Locate and identify every blood parasite.
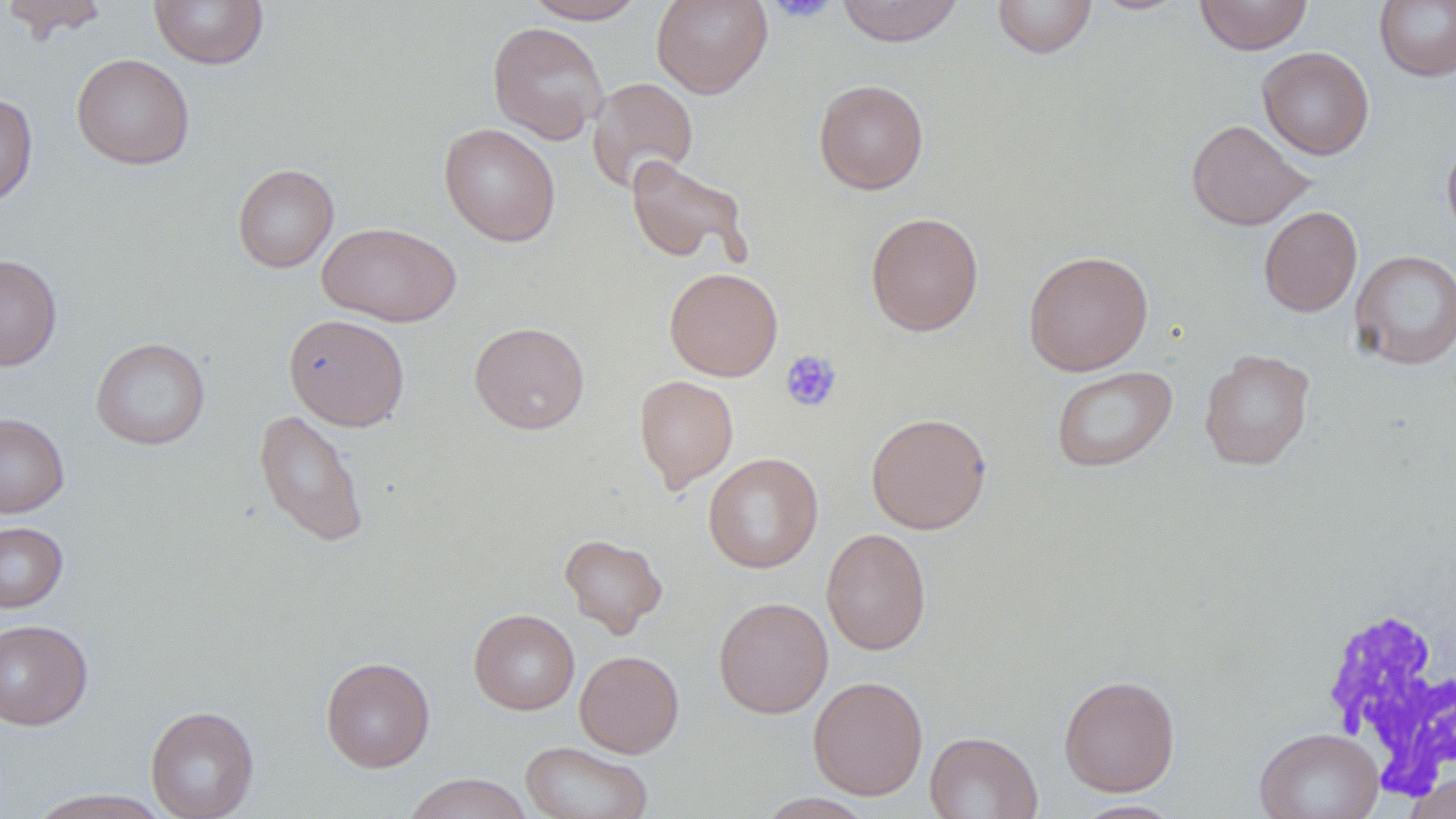

No blood parasites seen.

Approximate bounding boxes as [x1, y1, x2, y2] in pixels. White blood cell locations: [1320, 601, 1455, 800]. Uninfected red blood cell locations: [1, 0, 113, 41], [149, 0, 268, 69], [525, 0, 647, 23], [651, 0, 773, 98], [836, 0, 964, 47], [992, 0, 1097, 58], [1090, 0, 1193, 15], [1194, 0, 1312, 54], [1374, 0, 1456, 82], [487, 22, 608, 144], [1257, 47, 1374, 160], [71, 53, 195, 169], [586, 77, 698, 193], [814, 79, 928, 195], [0, 93, 38, 208], [1186, 119, 1313, 230], [439, 123, 560, 247], [1441, 133, 1456, 247], [625, 156, 751, 267], [233, 163, 339, 273], [1259, 206, 1362, 317], [865, 211, 984, 336], [317, 222, 462, 326], [1023, 250, 1154, 375], [1349, 250, 1456, 369], [0, 254, 62, 371], [664, 267, 783, 381], [283, 314, 410, 431], [469, 321, 590, 434], [91, 337, 210, 450], [1199, 349, 1315, 470], [1051, 365, 1177, 473], [634, 375, 738, 493], [254, 409, 369, 548], [865, 412, 992, 534], [0, 414, 69, 517], [703, 452, 823, 573], [0, 522, 68, 613], [821, 528, 931, 655], [559, 533, 668, 637], [713, 596, 833, 718], [469, 609, 580, 714], [0, 619, 93, 730], [574, 650, 685, 758], [321, 656, 435, 772], [1058, 674, 1180, 796], [807, 676, 928, 799], [145, 704, 258, 819], [1254, 727, 1384, 819], [925, 730, 1042, 819], [520, 741, 653, 819], [1404, 769, 1456, 819], [403, 772, 534, 819], [24, 789, 174, 818], [756, 793, 877, 818], [1070, 799, 1185, 818]. Platelet locations: [768, 0, 837, 22], [780, 349, 842, 412]. Slide-level diagnosis: negative for blood parasites. Image is 1456×819 pixels. Thin blood smear. May-Grünwald-Giemsa-stained preparation. Captured at 1000x magnification. Single field of view. Light microscopy.